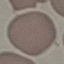

malaria status = uninfected
preparation = thin smear
image type = automatically extracted cell patch, resized to 64 × 64 pixels
capture = smartphone camera at the microscope eyepiece
stain = Giemsa